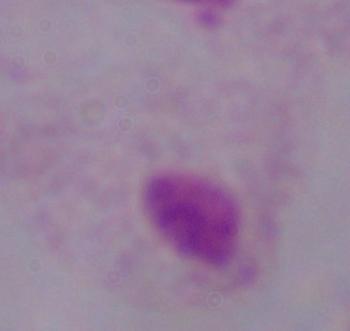

magnification: 1000x
identification: trichomonad
modality: micrograph